Assess this cell for malaria.
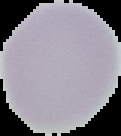
It is uninfected.

Summary:
  - Image size: 121×136 pixels
  - Preparation: thin blood smear
  - Image type: segmented cell region with the area outside set to black